Outline each blood parasite and name the species.
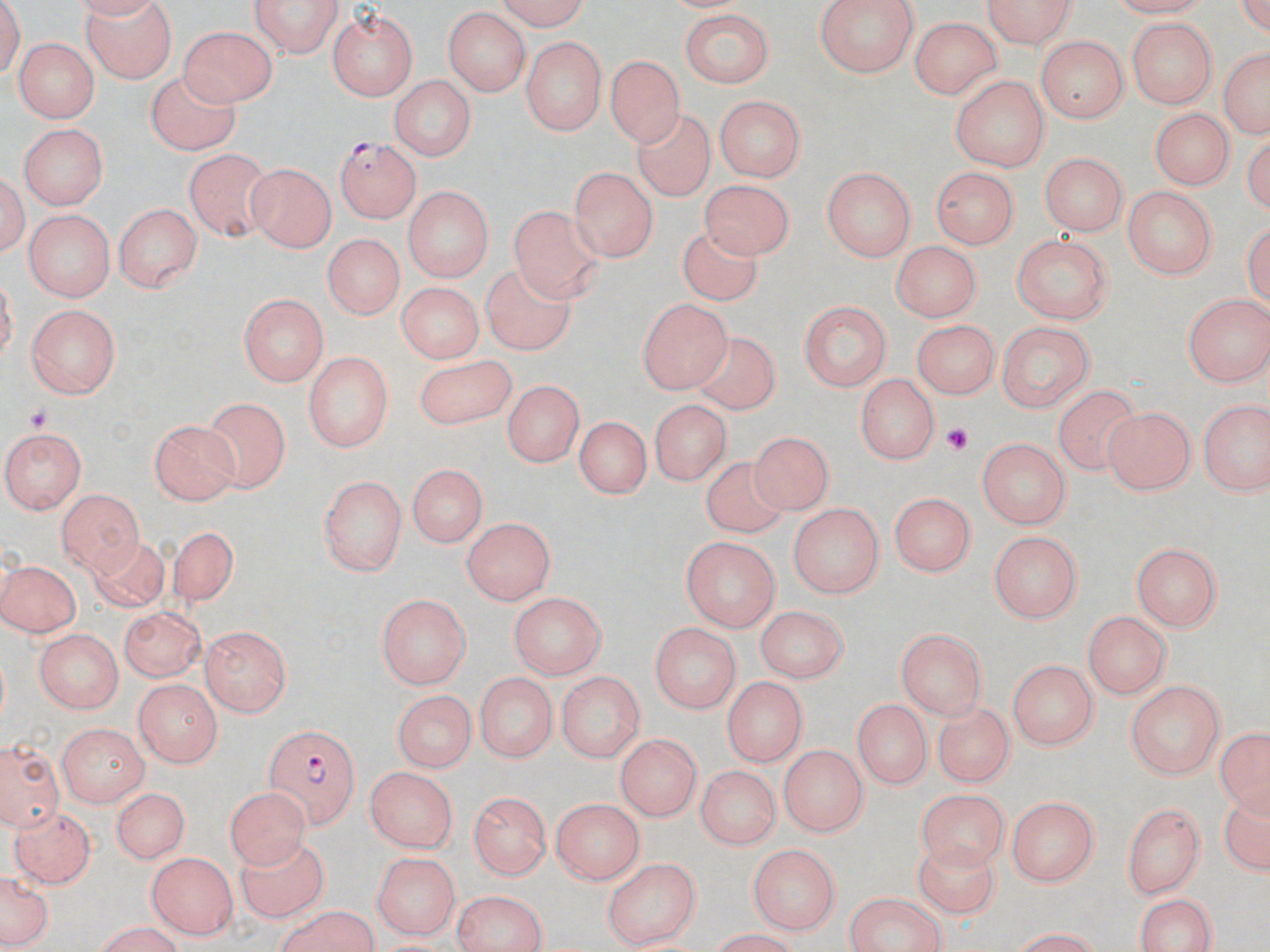
Approximate bounding boxes as [x1, y1, x2, y2] in pixels.
Plasmodium falciparum-infected red blood cells: [334, 136, 422, 222], [263, 725, 360, 829].
No Plasmodium ovale, Plasmodium malariae, Plasmodium vivax, Babesia divergens, or Trypanosoma brucei observed.

Platelet locations: [26, 404, 58, 434], [944, 422, 974, 454]. Uninfected red blood cell locations: [77, 0, 180, 81], [253, 0, 341, 58], [489, 0, 596, 28], [813, 0, 916, 76], [978, 0, 1080, 50], [327, 6, 418, 100], [442, 8, 527, 96], [675, 10, 779, 86], [911, 15, 1008, 99], [1125, 17, 1217, 110], [180, 25, 278, 106], [520, 35, 606, 134], [1034, 35, 1130, 121], [11, 39, 97, 122], [1217, 42, 1269, 142], [606, 54, 685, 146], [146, 65, 240, 152], [388, 74, 475, 162], [951, 76, 1048, 171], [715, 96, 804, 183], [1148, 108, 1232, 193], [633, 111, 716, 202], [19, 126, 106, 208], [184, 148, 274, 245], [1041, 152, 1128, 237], [244, 163, 337, 254], [569, 165, 656, 263], [821, 167, 914, 262], [927, 167, 1023, 246], [700, 180, 797, 263], [1124, 186, 1217, 280], [404, 187, 493, 285], [509, 197, 603, 299], [113, 199, 205, 294], [21, 208, 117, 300], [675, 226, 765, 303], [1013, 235, 1112, 324], [324, 236, 401, 321], [892, 242, 978, 323], [480, 267, 579, 357], [394, 281, 481, 365], [1183, 293, 1267, 385], [238, 294, 327, 384], [635, 297, 735, 393], [797, 301, 892, 392], [25, 304, 122, 398], [914, 318, 1002, 395], [994, 319, 1098, 410], [685, 328, 780, 413], [303, 349, 394, 453], [413, 350, 517, 430], [857, 373, 938, 465], [503, 380, 582, 468], [1051, 382, 1146, 474], [204, 395, 291, 494], [1198, 397, 1269, 494], [649, 399, 735, 482], [1102, 405, 1198, 494], [575, 414, 649, 501], [147, 419, 240, 504], [4, 427, 87, 514], [747, 432, 838, 516], [977, 437, 1069, 527], [704, 455, 791, 540], [404, 462, 489, 550], [320, 475, 406, 576], [55, 488, 145, 575], [889, 491, 973, 577], [790, 503, 882, 599], [461, 517, 556, 605], [167, 523, 241, 609], [991, 529, 1083, 623], [682, 536, 782, 631], [89, 538, 172, 611], [1131, 542, 1223, 633], [0, 557, 81, 640], [511, 591, 607, 678], [376, 592, 471, 691], [756, 605, 847, 681], [118, 606, 205, 679], [1083, 609, 1174, 700], [646, 620, 745, 712], [199, 626, 290, 713], [37, 628, 122, 714], [896, 629, 983, 719], [1007, 658, 1099, 748], [555, 670, 644, 761], [473, 671, 556, 763], [722, 676, 806, 768], [133, 678, 222, 765], [1127, 680, 1225, 781], [388, 688, 480, 771], [853, 697, 930, 792], [932, 702, 1015, 787], [55, 722, 146, 806], [1214, 723, 1268, 814], [613, 733, 704, 818], [3, 742, 59, 827], [780, 742, 869, 835], [697, 763, 779, 852], [366, 768, 460, 853], [108, 785, 192, 864], [225, 786, 312, 869], [916, 790, 1008, 872], [470, 791, 550, 880], [1221, 795, 1270, 883], [549, 796, 647, 881], [1005, 797, 1099, 885], [1122, 800, 1208, 899], [10, 802, 95, 884], [238, 837, 328, 927], [746, 841, 839, 933], [912, 844, 1003, 921], [146, 850, 238, 937], [371, 852, 460, 939], [603, 858, 702, 950], [0, 871, 54, 952], [449, 891, 549, 952], [842, 892, 948, 952], [1133, 892, 1224, 951], [268, 908, 382, 952], [82, 923, 189, 950], [1004, 927, 1108, 951]. Slide-level diagnosis: Plasmodium falciparum. Thin blood film. Optical microscopy. One field of a larger specimen. May-Grünwald-Giemsa-stained preparation. Captured at 1000x magnification. Image is 1270×952 pixels.